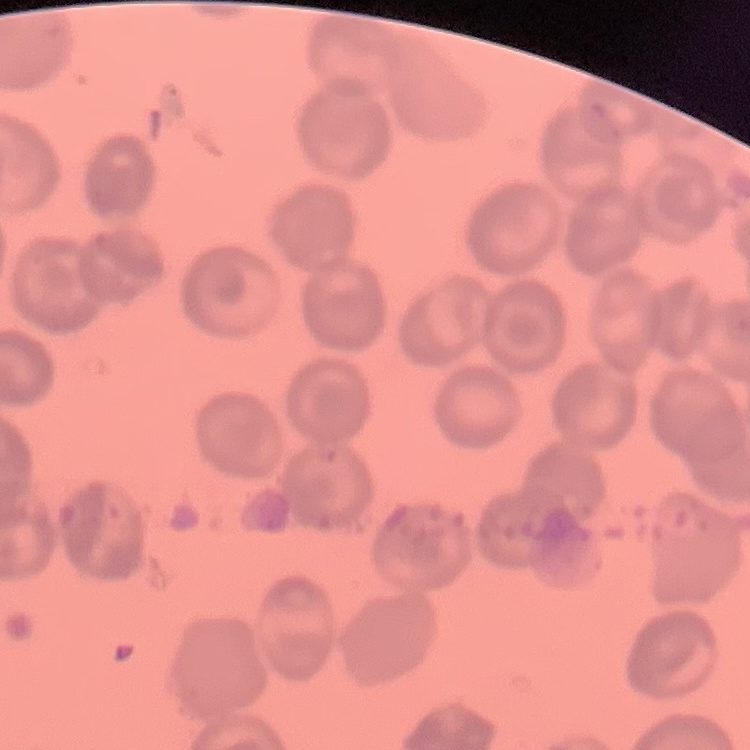
The red blood cells exhibit no rouleaux formation. Field's or Giemsa stain. Thin blood film. One tile cut from a larger photomicrograph.